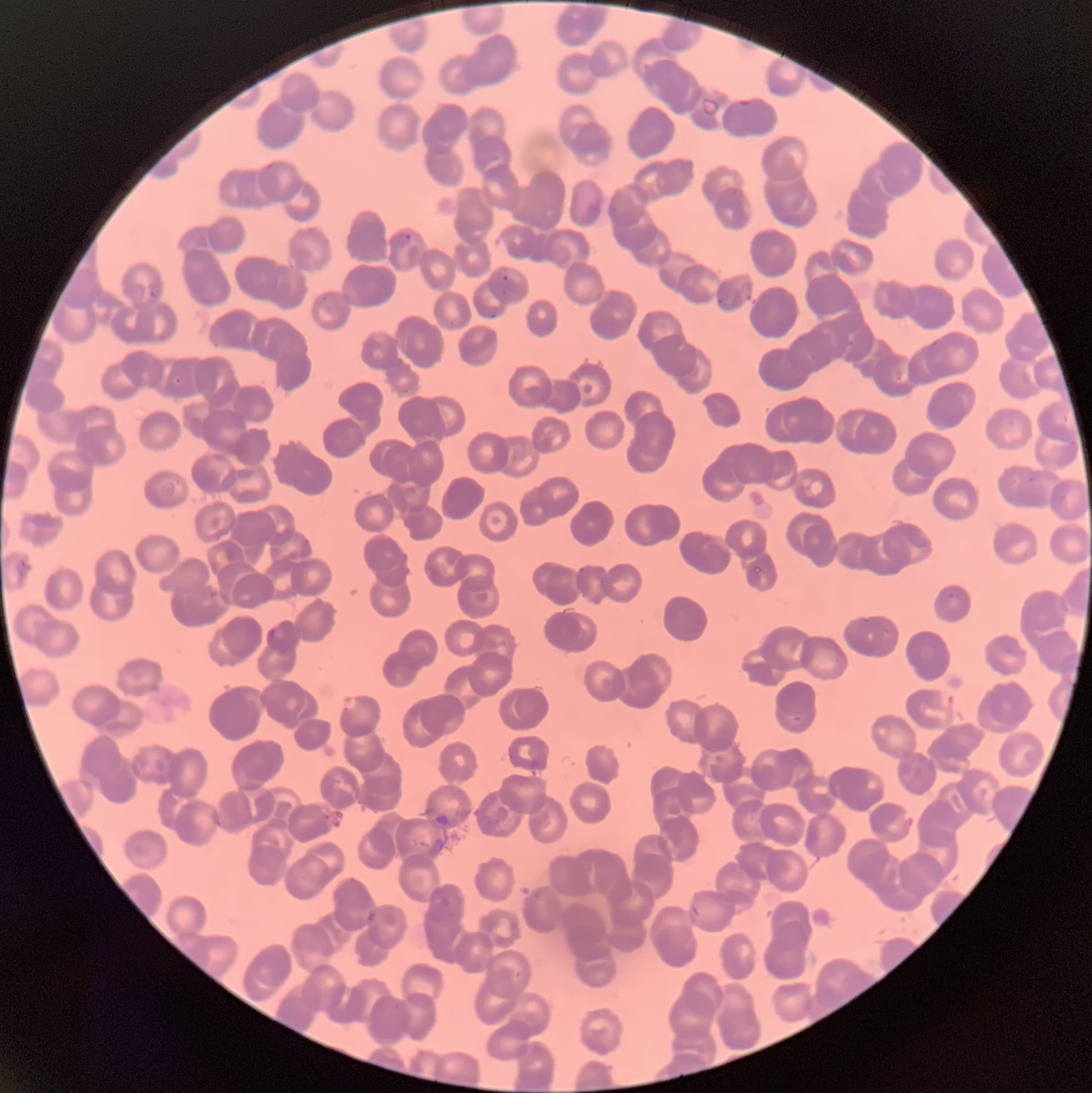
image_size: 1092×1093 pixels
modality: light microscopy
plasmodium_parasite_locations: 'approximate bounding boxes as [x1, y1, x2, y2] in pixels: [736, 98, 751, 108], [394, 233, 412, 248], [501, 274, 509, 282], [718, 298, 725, 306], [487, 310, 498, 319], [264, 627, 285, 646], [939, 689, 956, 710], [341, 695, 360, 711], [367, 909, 378, 922]'
preparation: thin blood smear
red_blood_cell_morphology: rouleaux formation